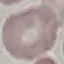

result = no malaria parasites seen
preparation = thin blood smear
capture = smartphone camera at the microscope eyepiece
image type = cell patch, automatically extracted from a larger field of view and resized to 64 × 64 pixels
stain = Giemsa